Identify the parasite.
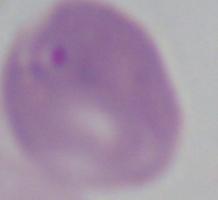

Babesia.

modality = micrograph
magnification = 1000x